State the preparation type.
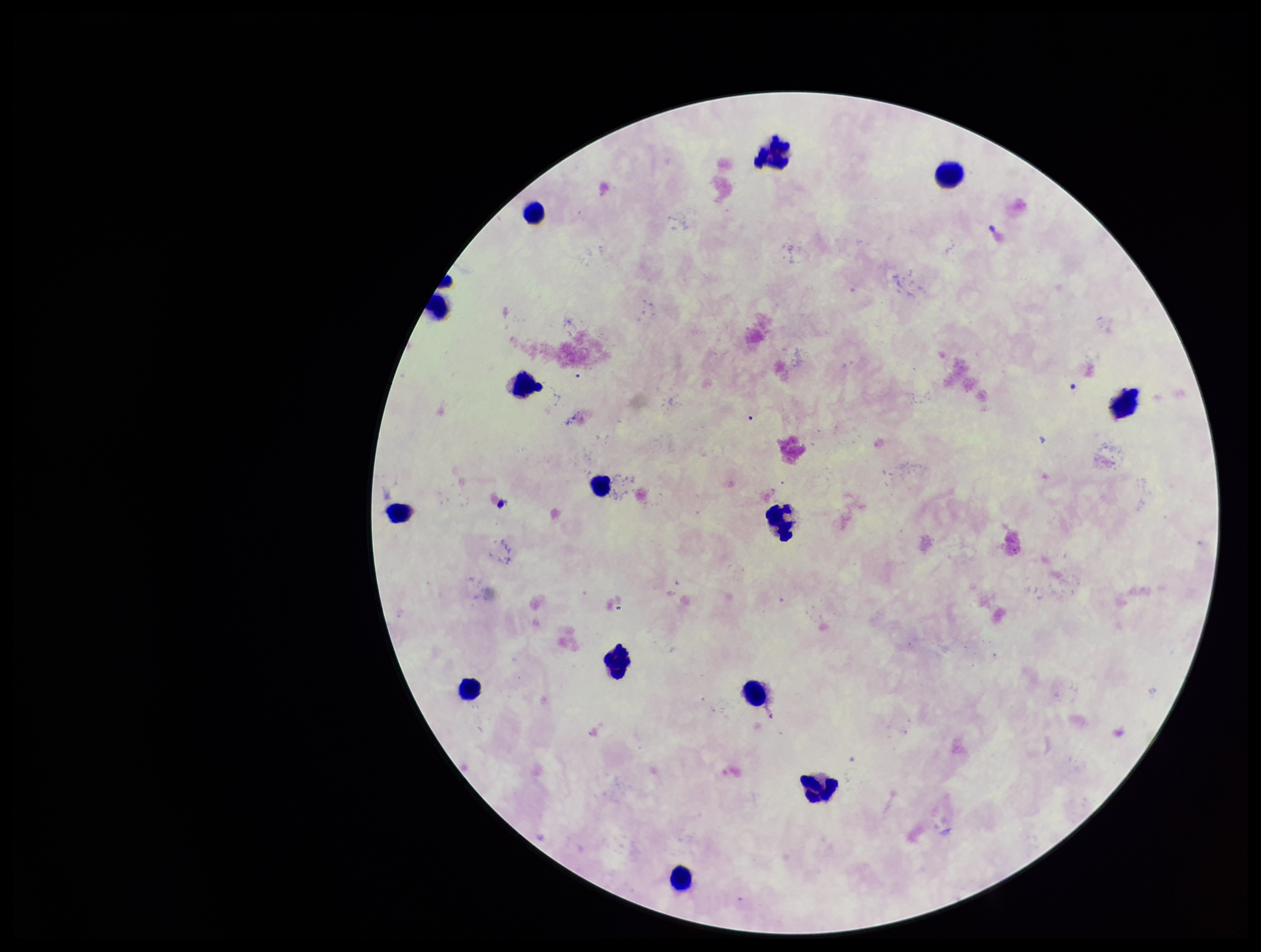

A thick smear.

Plasmodium parasites = none detected
field of view = one from this slide
capture = smartphone photograph through the microscope eyepiece
leukocyte count = 14
stain = Giemsa
image size = 1261×952 pixels
patient malaria status = negative
parasite count = 0